Name the parasite shown.
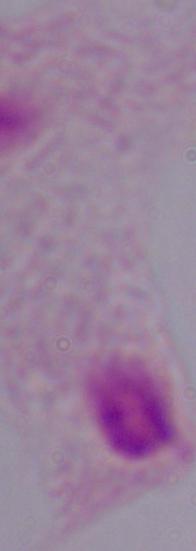

This is a trichomonad.

1000x magnification. Photomicrograph.